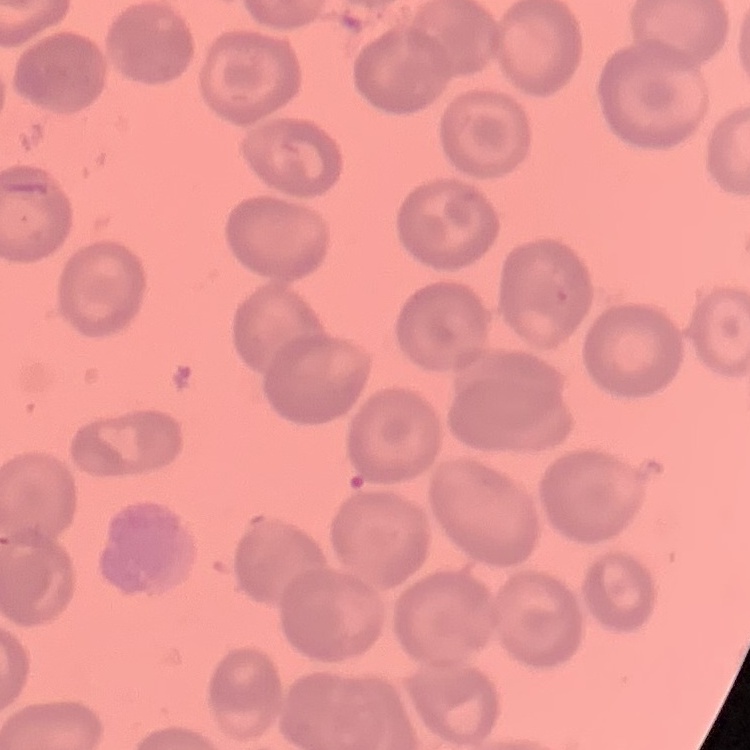
The red blood cells show no rouleaux formation. One tile cut from a larger photomicrograph. Thin blood smear. Stained with either Field's or Giemsa.